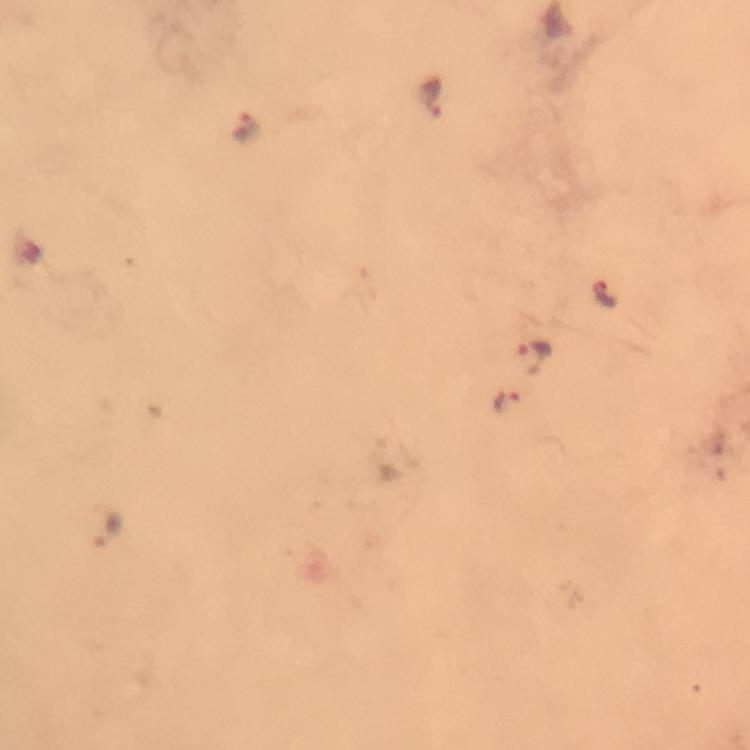

Approximate object centers, in pixels from the top-left corner. Plasmodium parasite locations: (x=436, y=96), (x=247, y=127), (x=604, y=293), (x=536, y=356), (x=508, y=400), (x=106, y=526). At 100x magnification. Image is 750×750 pixels. Smartphone photograph taken through a microscope. Giemsa stain. A crop from one field of view. Thick blood smear. Immersion oil was used. From a diagnostic examination for malaria.